Assess this cell for malaria.
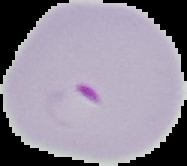

It is parasitized.

image size = 187×166 pixels
preparation = thin blood film
image type = cell region segmented out of the field of view; surrounding area masked to black